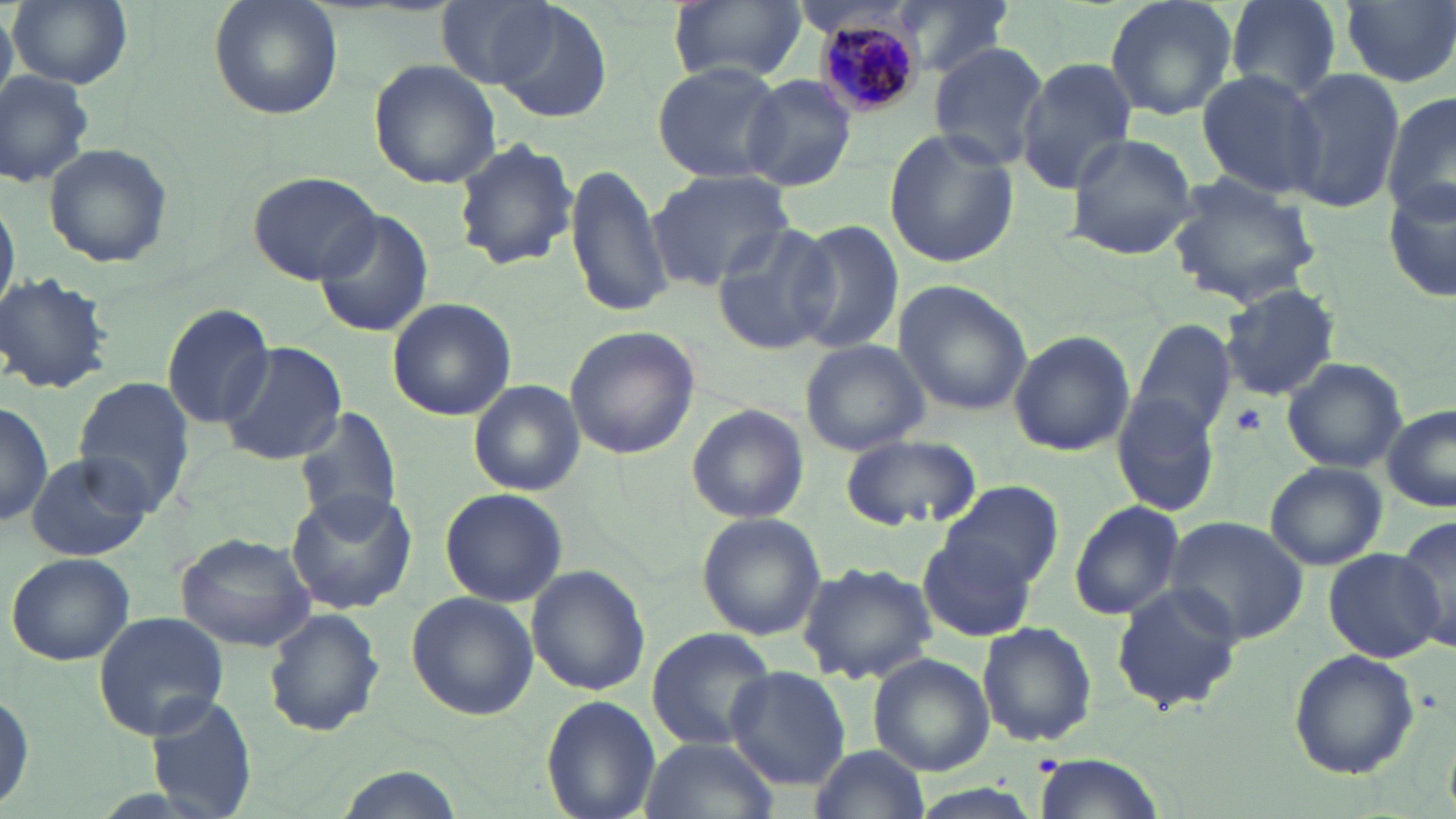

Summary:
  - Coordinate format: approximate bounding boxes as (x1, y1, x2, y2) in pixels
  - Platelet locations: (1233, 403, 1267, 434)
  - Plasmodium malariae-infected red blood cell locations: (815, 7, 927, 115)
  - Uninfected red blood cell locations: (8, 0, 133, 88), (209, 0, 344, 121), (892, 0, 1015, 79), (1102, 0, 1239, 122), (1221, 0, 1346, 102), (435, 1, 558, 89), (666, 1, 807, 86), (487, 2, 613, 125), (1342, 2, 1455, 88), (927, 41, 1049, 170), (1017, 57, 1139, 190), (368, 60, 500, 188), (650, 60, 788, 183), (1196, 69, 1324, 198), (1277, 69, 1406, 214), (0, 70, 94, 188), (741, 74, 857, 191), (1383, 95, 1456, 224), (882, 129, 1019, 270), (1062, 132, 1200, 260), (452, 136, 580, 271), (41, 140, 173, 269), (565, 159, 674, 320), (645, 167, 798, 291), (247, 170, 381, 284), (1168, 175, 1324, 304), (1385, 180, 1456, 307), (0, 190, 18, 323), (313, 208, 434, 339), (790, 221, 906, 356), (711, 223, 842, 356), (0, 273, 113, 394), (891, 279, 1033, 417), (1219, 285, 1341, 400), (387, 298, 516, 422), (159, 303, 278, 429), (1131, 319, 1238, 438), (564, 325, 699, 462), (1007, 330, 1135, 458), (799, 339, 930, 455), (217, 341, 347, 467), (1280, 356, 1408, 474), (468, 378, 585, 497), (72, 379, 195, 511), (1111, 389, 1222, 519), (0, 399, 51, 530), (295, 402, 404, 524), (686, 404, 809, 525), (1381, 404, 1456, 512), (841, 434, 981, 531), (23, 451, 154, 562), (1265, 463, 1388, 570), (941, 478, 1065, 595), (439, 487, 567, 607), (284, 488, 417, 614), (1068, 498, 1187, 621), (695, 512, 825, 642), (1164, 516, 1310, 646), (1393, 516, 1456, 656), (175, 532, 316, 652), (918, 537, 1038, 641), (1321, 549, 1444, 661), (5, 551, 136, 666), (795, 560, 937, 686), (526, 564, 650, 695), (1109, 582, 1244, 716), (404, 590, 539, 721), (262, 608, 385, 738), (92, 611, 228, 737), (976, 621, 1098, 748), (645, 626, 777, 752), (1287, 648, 1420, 779), (867, 654, 994, 776), (724, 666, 850, 791), (0, 684, 35, 814), (146, 693, 254, 817), (541, 695, 661, 819), (638, 734, 779, 819), (807, 743, 930, 819), (1033, 751, 1165, 819), (907, 785, 1045, 819)
  - Slide-level diagnosis: Plasmodium malariae
  - Modality: optical microscopy
  - Stain: May-Grünwald-Giemsa
  - Magnification: 1000x
  - Field of view: single
  - Image size: 1456×819 pixels
  - Preparation: thin blood film